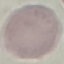
Result: negative for malaria parasites. Thin blood film. Acquired by smartphone through the microscope eyepiece. Giemsa stain. Automatically extracted cell patch, resized to 64 × 64 pixels.